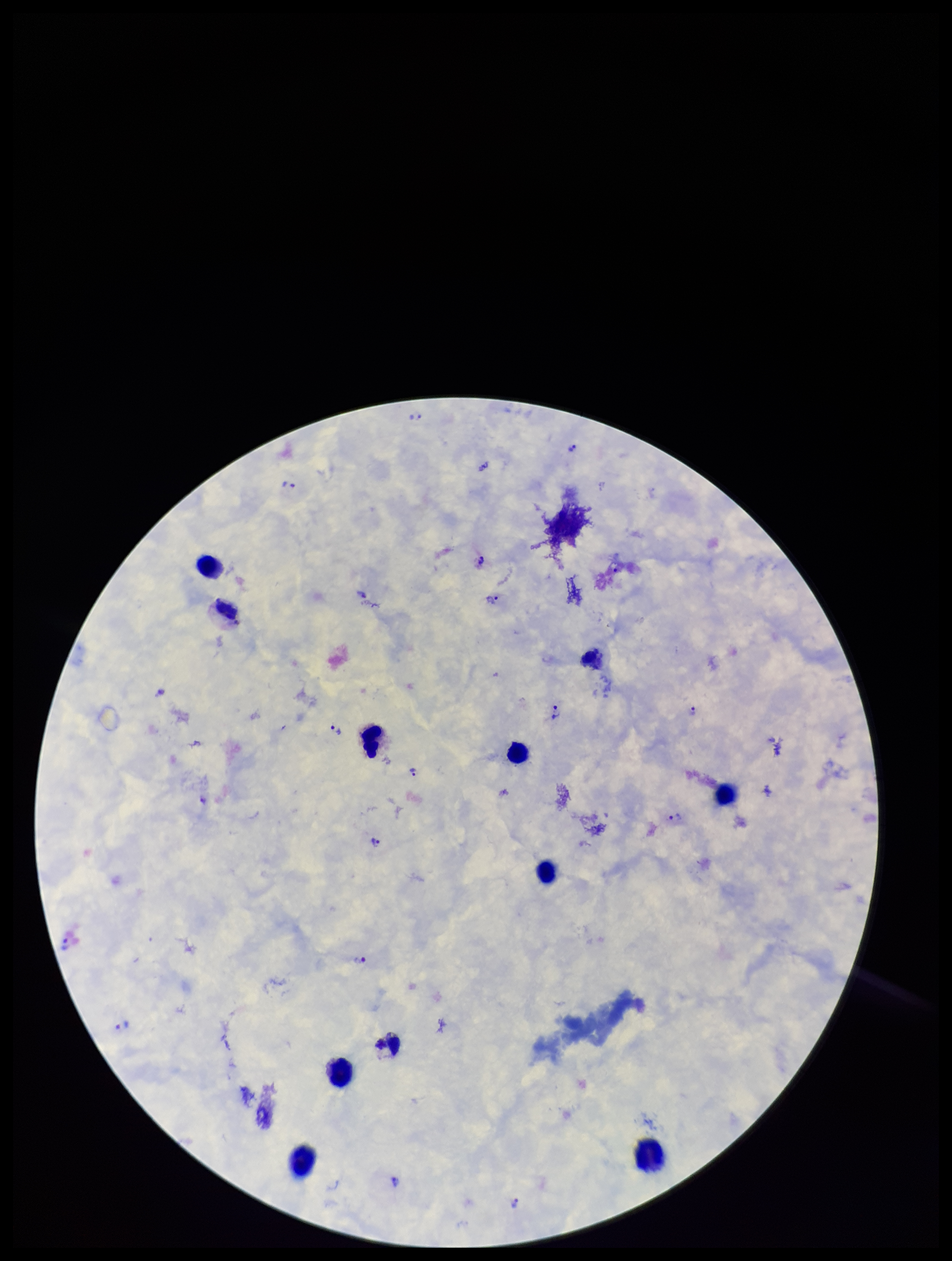

Summary:
  - Field of view: one from this slide
  - Stain: Giemsa
  - Species reported for this patient: Plasmodium vivax
  - Preparation: thick
  - Plasmodium parasites: detected
  - Patient malaria status: positive
  - Leukocyte count: 11
  - Image size: 952×1261 pixels
  - Capture: smartphone photograph through the microscope eyepiece
  - Parasite count: 20